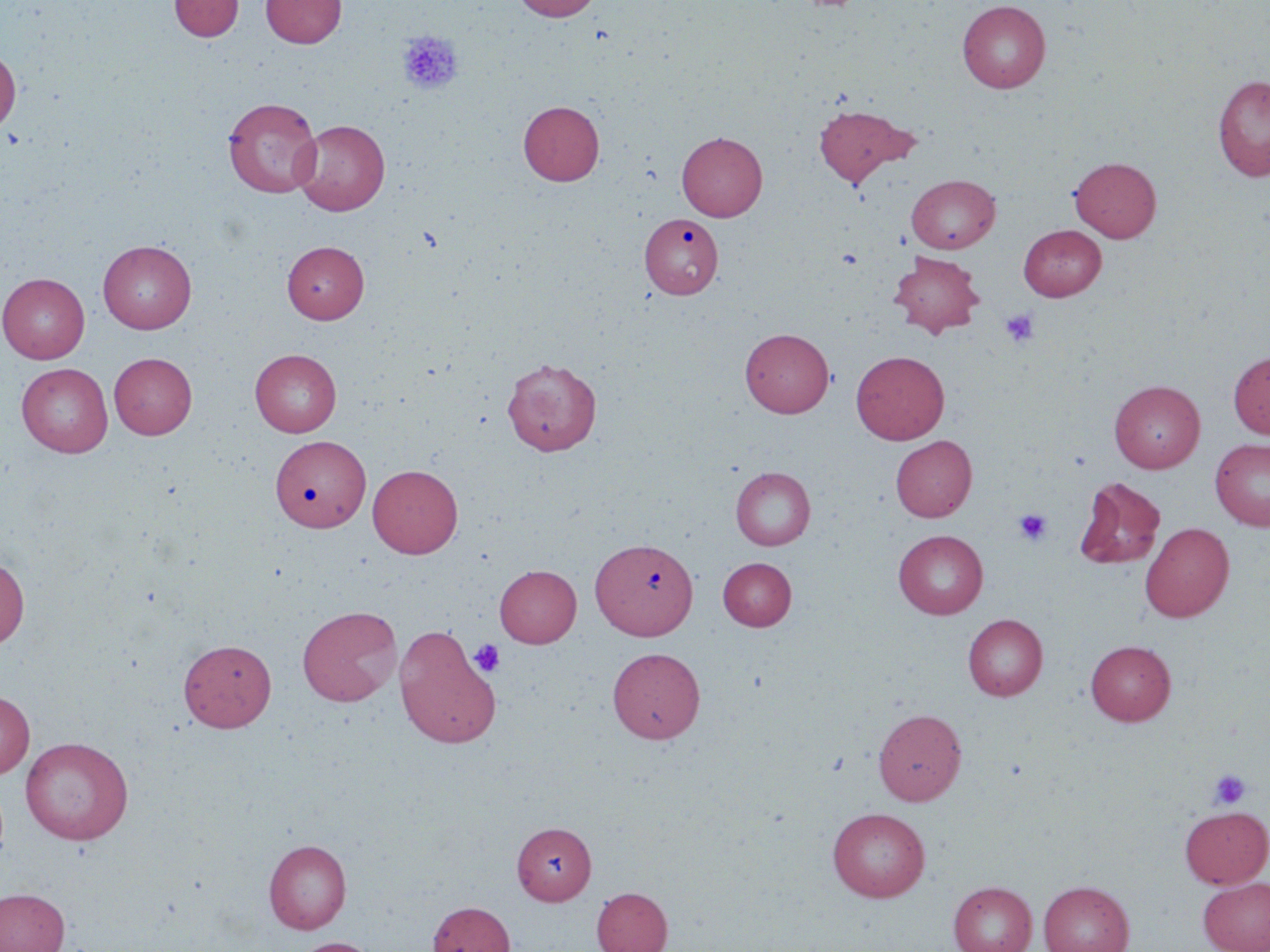
slide-level diagnosis = negative for blood parasites
uninfected red blood cell locations = approximate bounding boxes as (x1,y1)-(x2,y2) corner pairs in pixels: (169,0)-(244,41), (261,0)-(346,47), (513,0)-(601,21), (957,0)-(1051,92), (0,48)-(21,133), (1212,75)-(1270,180), (223,97)-(322,198), (519,100)-(604,185), (813,103)-(918,186), (293,120)-(390,215), (677,131)-(767,220), (1070,156)-(1161,242), (906,174)-(1000,253), (641,212)-(725,299), (1019,225)-(1106,300), (98,240)-(197,333), (282,241)-(368,324), (889,251)-(986,338), (0,273)-(89,364), (741,327)-(834,417), (250,349)-(342,436), (851,350)-(949,444), (1229,351)-(1270,439), (109,352)-(197,439), (501,357)-(602,456), (16,363)-(113,457), (1109,380)-(1205,472), (270,434)-(370,531), (890,435)-(976,521), (1210,437)-(1270,531), (367,464)-(463,557), (730,466)-(815,550), (1074,477)-(1166,569), (1140,522)-(1234,622), (894,530)-(988,619), (591,537)-(697,640), (0,557)-(29,649), (718,557)-(796,630), (495,565)-(581,647), (297,605)-(402,706), (963,614)-(1048,700), (394,627)-(500,749), (178,638)-(275,732), (1085,640)-(1176,725), (608,647)-(705,743), (0,690)-(34,779), (873,708)-(967,805), (20,737)-(133,844), (1180,806)-(1270,887), (827,807)-(930,902), (512,822)-(597,904), (263,840)-(351,934), (1198,877)-(1270,952), (949,881)-(1037,952), (1038,881)-(1134,952), (591,887)-(672,952), (0,888)-(70,952), (428,901)-(516,952), (291,937)-(380,952)
magnification = 1000x
preparation = thin blood smear
platelet locations = approximate bounding boxes as (x1,y1)-(x2,y2) corner pairs in pixels: (397,30)-(462,95), (1000,309)-(1038,346), (1014,508)-(1052,545), (470,639)-(505,678), (1209,769)-(1252,808)
stain = May-Grünwald-Giemsa
image size = 1270×952 pixels
field of view = single
modality = light microscopy